State which parasite is depicted.
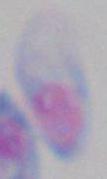
Toxoplasma gondii.

Captured at 1000x magnification. Micrograph.